Name the parasite shown.
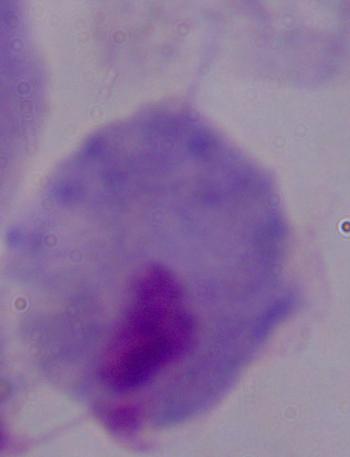
This is a trichomonad.

modality: photomicrograph
magnification: 1000x